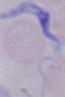
Summary:
  - Modality: micrograph
  - Identification: trypanosome
  - Magnification: 1000x